Report the malaria status of this cell.
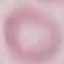
It is uninfected.

Summary:
  - Capture: smartphone through the microscope eyepiece
  - Stain: Giemsa
  - Image type: automatically extracted cell patch, resized to 64 × 64 pixels
  - Preparation: thin smear